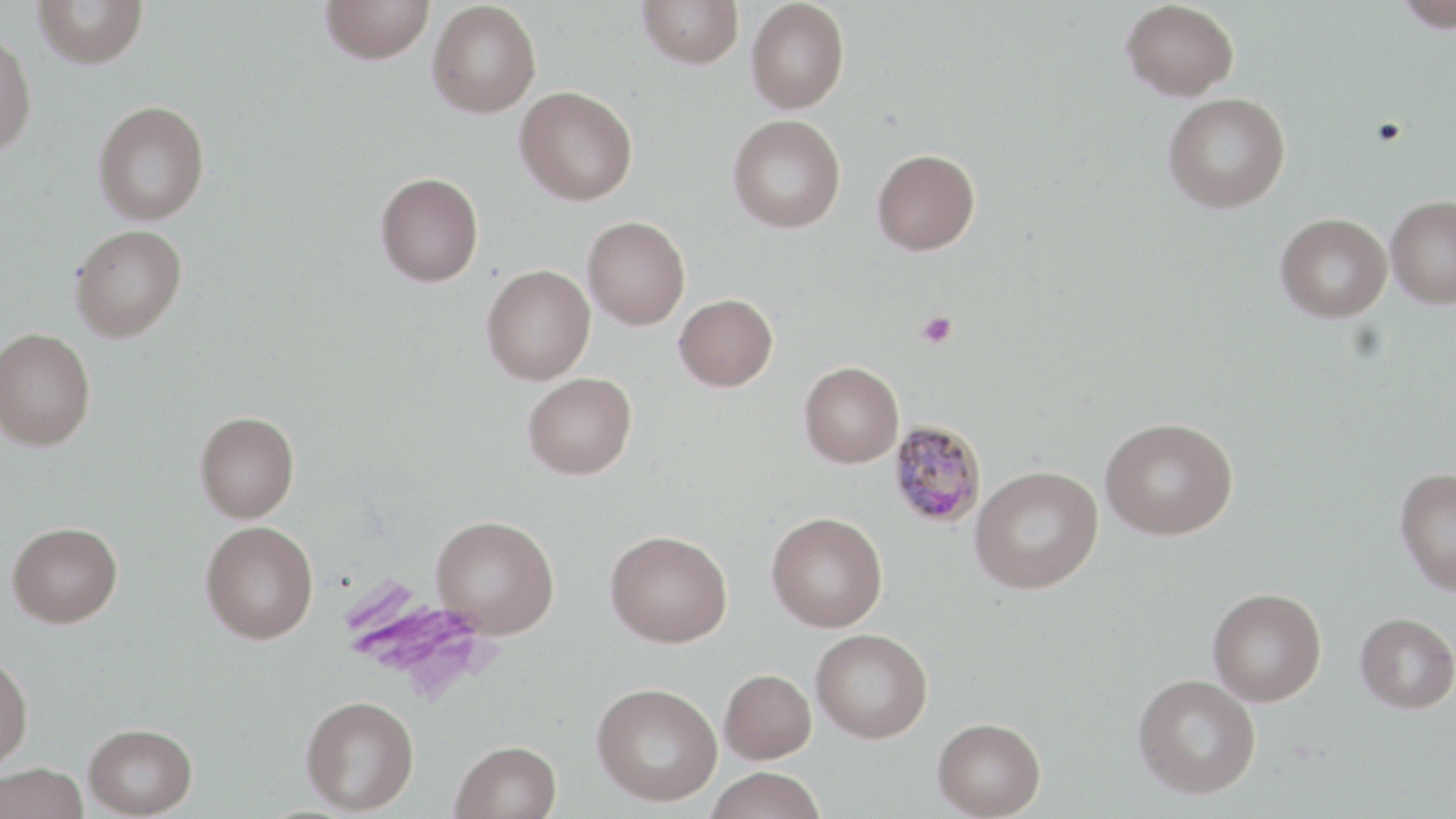
Approximate bounding boxes as (x1,y1)-(x2,y2) corner pairs in pixels. Uninfected red blood cell locations: (32,0)-(148,69), (320,0)-(435,64), (638,0)-(744,69), (745,0)-(849,113), (1121,0)-(1239,101), (1394,0)-(1456,33), (426,1)-(542,117), (0,30)-(38,157), (515,85)-(638,205), (1163,93)-(1291,213), (93,99)-(210,225), (728,114)-(846,233), (872,148)-(980,254), (375,172)-(484,287), (1386,194)-(1456,309), (1276,213)-(1392,322), (583,216)-(690,329), (70,224)-(187,342), (482,264)-(595,384), (673,294)-(778,391), (0,327)-(96,451), (799,361)-(904,467), (523,372)-(636,479), (194,410)-(300,522), (1101,417)-(1238,540), (970,465)-(1103,594), (1394,466)-(1456,595), (766,512)-(888,632), (431,515)-(559,638), (7,521)-(123,627), (201,521)-(318,644), (606,529)-(732,647), (1208,587)-(1326,706), (1355,613)-(1456,713), (811,628)-(933,743), (0,653)-(33,773), (719,669)-(816,764), (1133,674)-(1260,799), (592,682)-(723,806), (300,695)-(419,814), (932,717)-(1046,818), (84,723)-(198,817), (450,740)-(562,819), (0,762)-(88,819), (704,767)-(827,819). Platelet locations: (917,311)-(958,348). Plasmodium malariae-infected red blood cell locations: (888,421)-(987,528). Slide-level diagnosis: Plasmodium malariae. Image is 1456×819 pixels. 1000x magnification. Optical microscopy. One field of a larger specimen. Thin blood smear. May-Grünwald-Giemsa stain.